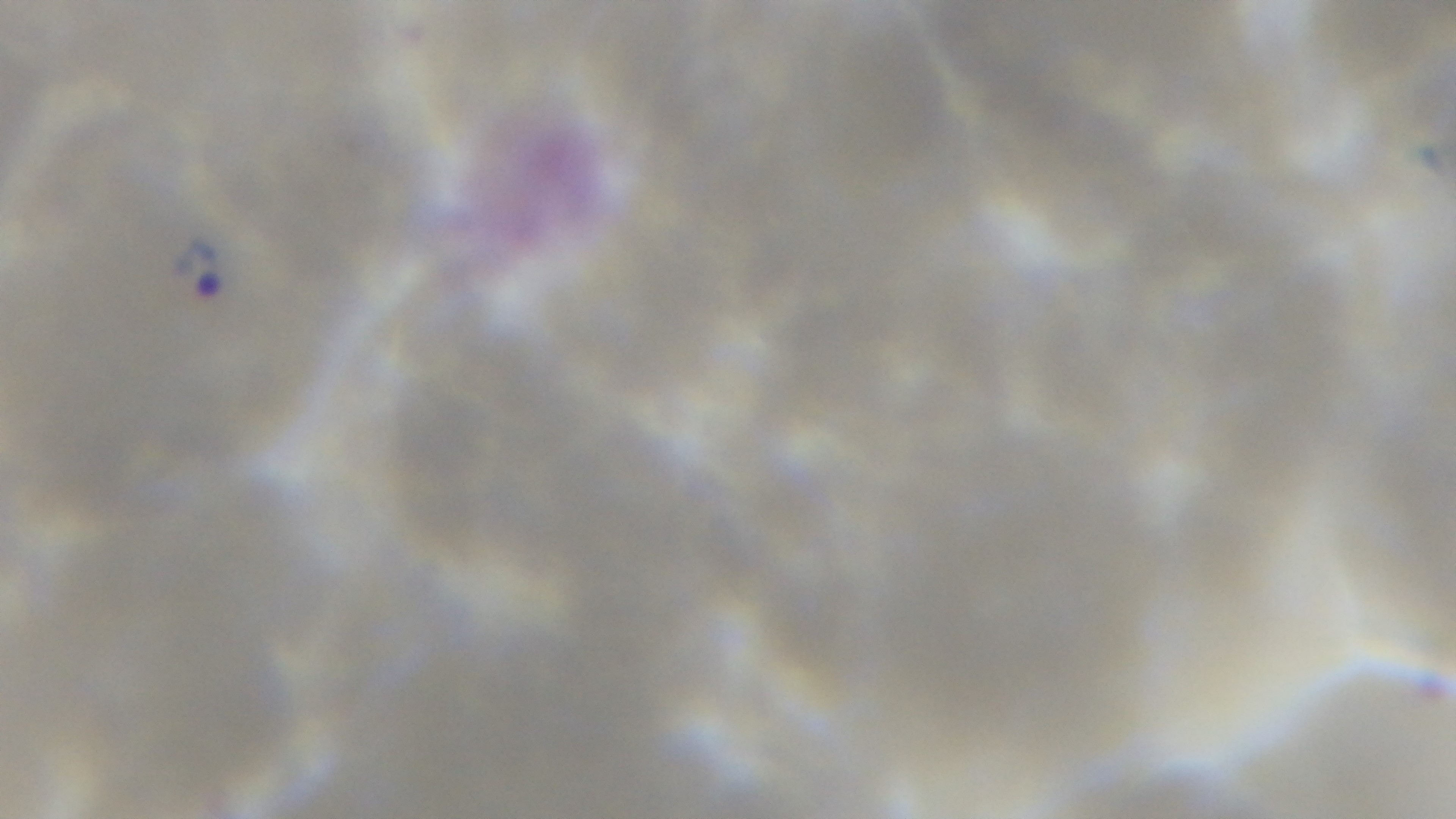

Summary:
  - Stain: Giemsa
  - Capture: mounted 4K digital camera
  - Malaria status: positive
  - Field of view: single
  - Objective: 100x oil immersion
  - Preparation: thin blood film
  - Modality: light microscopy